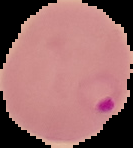

image_size: 133×148 pixels
image_type: cell region segmented out of the field of view; surrounding area masked to black
result: Plasmodium parasites identified
preparation: thin blood film